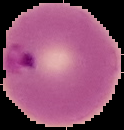

From a thin blood film. Image is 124×130 pixels. Segmented cell region on a black background. Malaria status: parasitized.